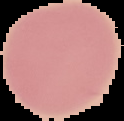

image_size: 124×121 pixels
image_type: cell region segmented out of the field of view; surrounding area masked to black
preparation: thin blood smear
malaria_status: uninfected